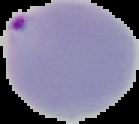 From a thin blood film. The area outside the segmented cell region is set to black. Image is 139×124 pixels. Malaria status: parasitized.